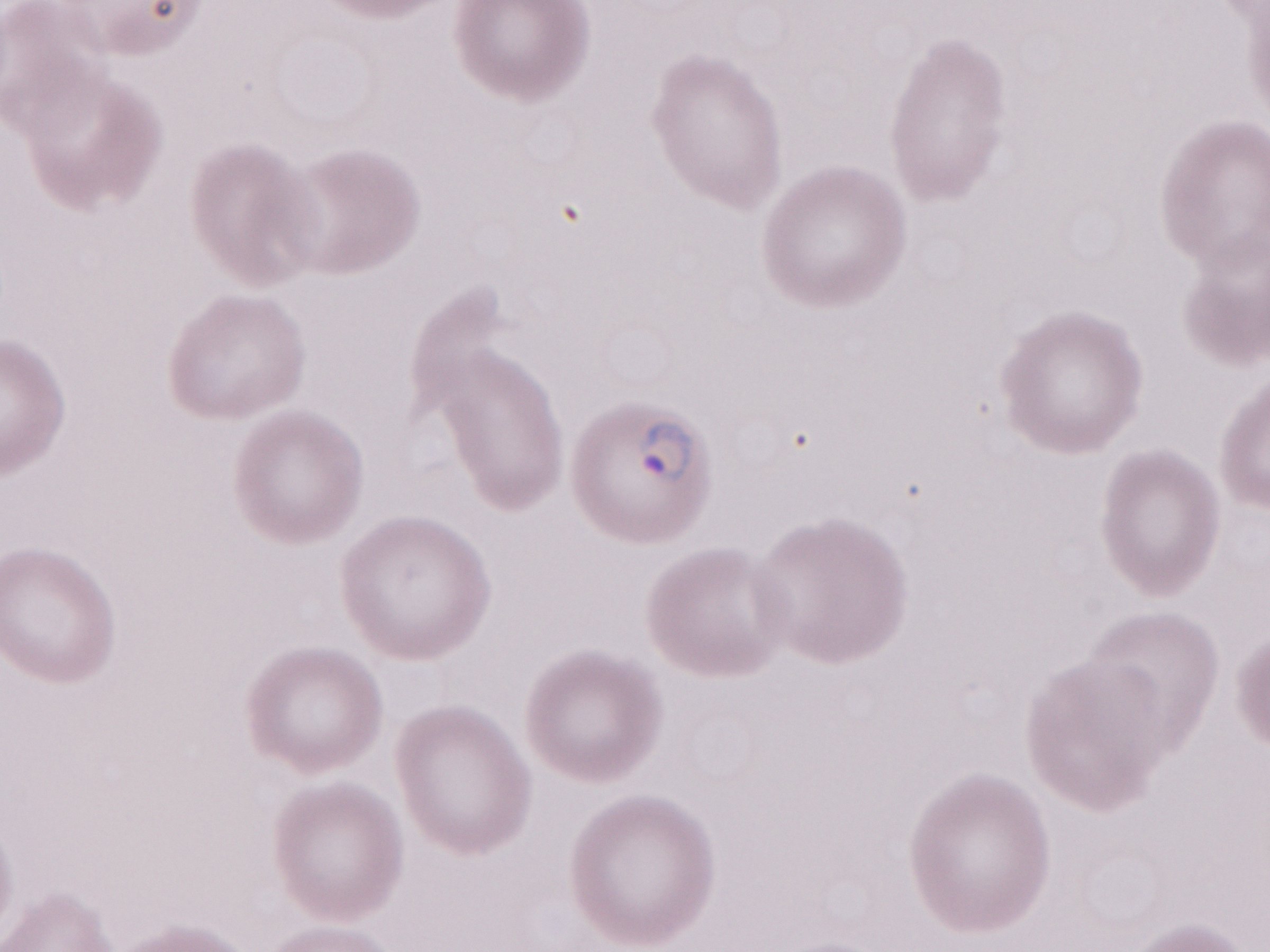 May-Grünwald-Giemsa-stained preparation. Patient diagnosis: malaria infection. Single field of view. Olympus BX43 microscope and DP73 digital camera. Magnification: 1,000x. Image is 1270×952 pixels. Thin blood film.